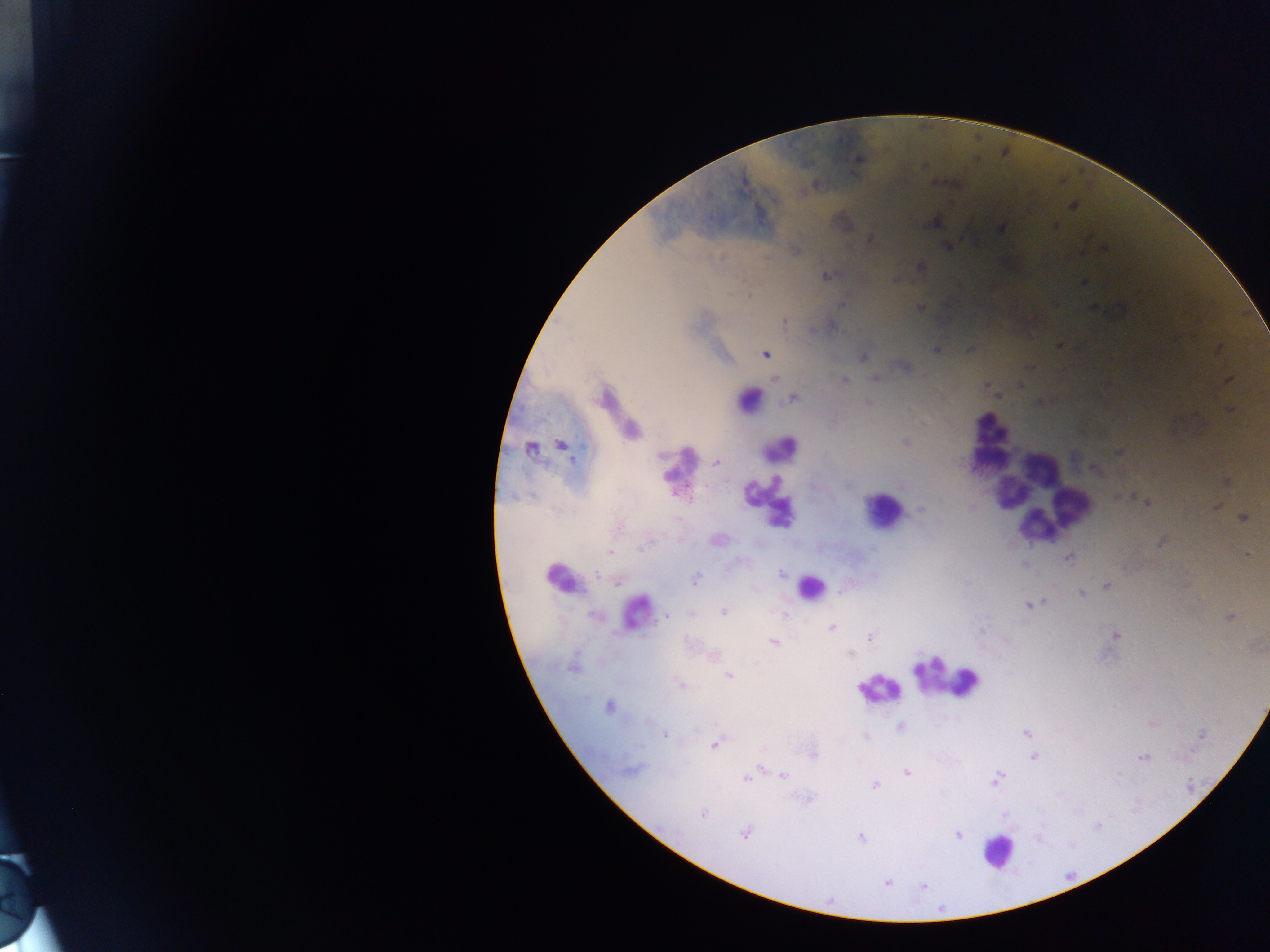 Approximate centers as x y in pixels. Leukocyte locations: 992 425; 781 447; 990 459; 1041 464; 1009 494; 1067 495; 886 505; 778 515; 1033 528; 811 587; 947 679; 880 692; 997 853. Malaria parasite locations: 857 164; 813 186; 933 222; 1003 231; 868 237; 949 248; 921 265; 825 276; 1084 283; 843 304; 920 308; 783 320; 833 325; 1058 346; 936 349; 767 355; 862 356; 876 377; 774 378; 845 379; 749 398; 792 399; 867 401; 1228 411; 906 442; 561 445; 528 449; 661 456; 717 463; 773 480; 1225 482; 752 486; 1147 503; 1213 505; 921 512; 1243 518; 1162 542; 636 550; 610 552; 1245 553; 1068 559; 782 572; 596 575; 556 577; 694 578; 616 582; 1107 585; 1082 594; 1028 605; 723 612; 692 615; 665 616; 669 616; 1228 616; 831 628; 870 636; 773 642; 850 654; 918 669; 730 676; 681 685; 609 707; 649 720; 666 736; 714 745; 1142 758; 758 766; 637 770; 908 772; 782 775; 745 781; 876 785; 702 813; 1096 826; 744 834; 959 835; 860 837; 1037 837; 887 883; 925 886. One field of view. Image is 1270×952 pixels. Thick blood smear. Sample from Ghana. Photographed through a microscope with a mobile-phone camera.